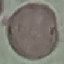
Summary:
  - Result: no malaria parasites detected
  - Capture: smartphone through the microscope eyepiece
  - Image type: automatically extracted cell patch, resized to 64 × 64 pixels
  - Stain: Giemsa
  - Preparation: thin blood smear